Locate and identify every blood parasite.
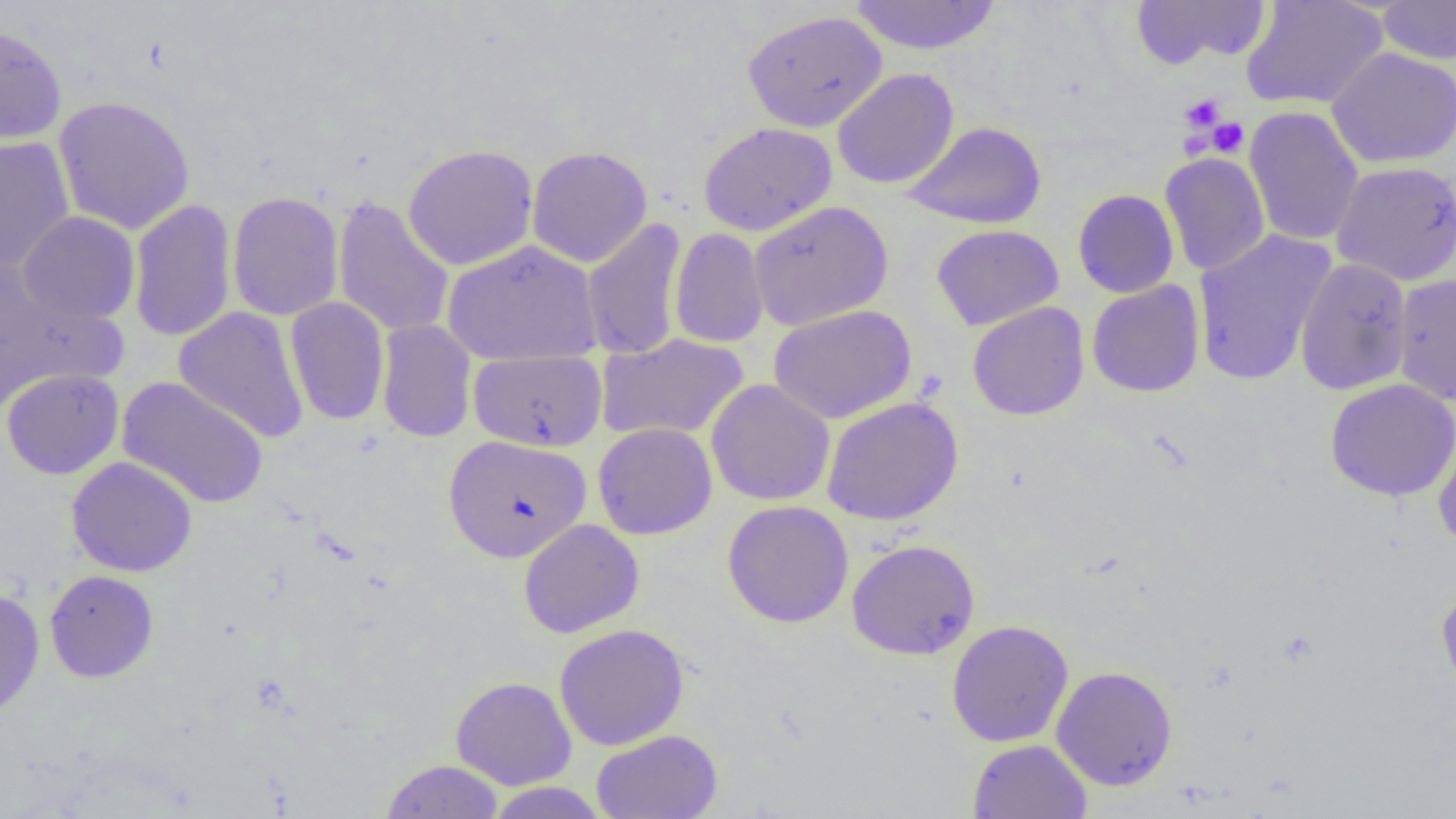
No blood parasites observed.

Approximate bounding boxes as (x1,y1)-(x2,y2) corner pairs in pixels. Uninfected red blood cell locations: (848,0)-(1002,55), (1241,0)-(1388,111), (1129,1)-(1272,71), (1375,1)-(1456,65), (742,10)-(887,133), (0,23)-(67,146), (1326,48)-(1456,168), (832,68)-(960,190), (52,95)-(195,236), (1243,106)-(1364,247), (903,121)-(1047,230), (699,122)-(837,236), (0,136)-(75,273), (403,144)-(539,270), (526,146)-(653,268), (1159,153)-(1270,276), (1331,161)-(1456,286), (1072,189)-(1179,298), (227,191)-(344,321), (332,196)-(454,339), (128,198)-(237,343), (749,200)-(893,332), (17,211)-(140,325), (582,217)-(688,361), (932,224)-(1064,330), (669,228)-(769,348), (1191,230)-(1336,386), (442,239)-(602,367), (1294,257)-(1413,395), (0,267)-(128,408), (1393,274)-(1456,405), (1086,280)-(1205,397), (285,297)-(390,426), (967,302)-(1090,421), (768,305)-(917,424), (173,306)-(310,444), (376,320)-(477,444), (596,334)-(748,442), (469,350)-(607,452), (1,368)-(124,480), (117,376)-(269,509), (706,379)-(835,506), (1324,379)-(1456,502), (821,397)-(964,526), (1433,419)-(1456,550), (592,422)-(718,540), (443,434)-(592,562), (66,457)-(198,577), (722,500)-(854,628), (518,519)-(645,638), (846,539)-(980,660), (45,570)-(159,683), (1436,586)-(1456,699), (0,588)-(45,719), (946,619)-(1073,747), (554,623)-(689,750), (1051,665)-(1178,791), (450,676)-(577,790), (590,729)-(722,819), (967,739)-(1092,819), (380,759)-(505,818), (485,782)-(609,818). Platelet locations: (1180,94)-(1226,133), (1207,116)-(1249,158), (1180,133)-(1208,160). Slide-level diagnosis: no evidence of blood parasites. Image is 1456×819 pixels. One field of a larger specimen. Captured at 1000x magnification. Optical microscopy. Thin blood film.